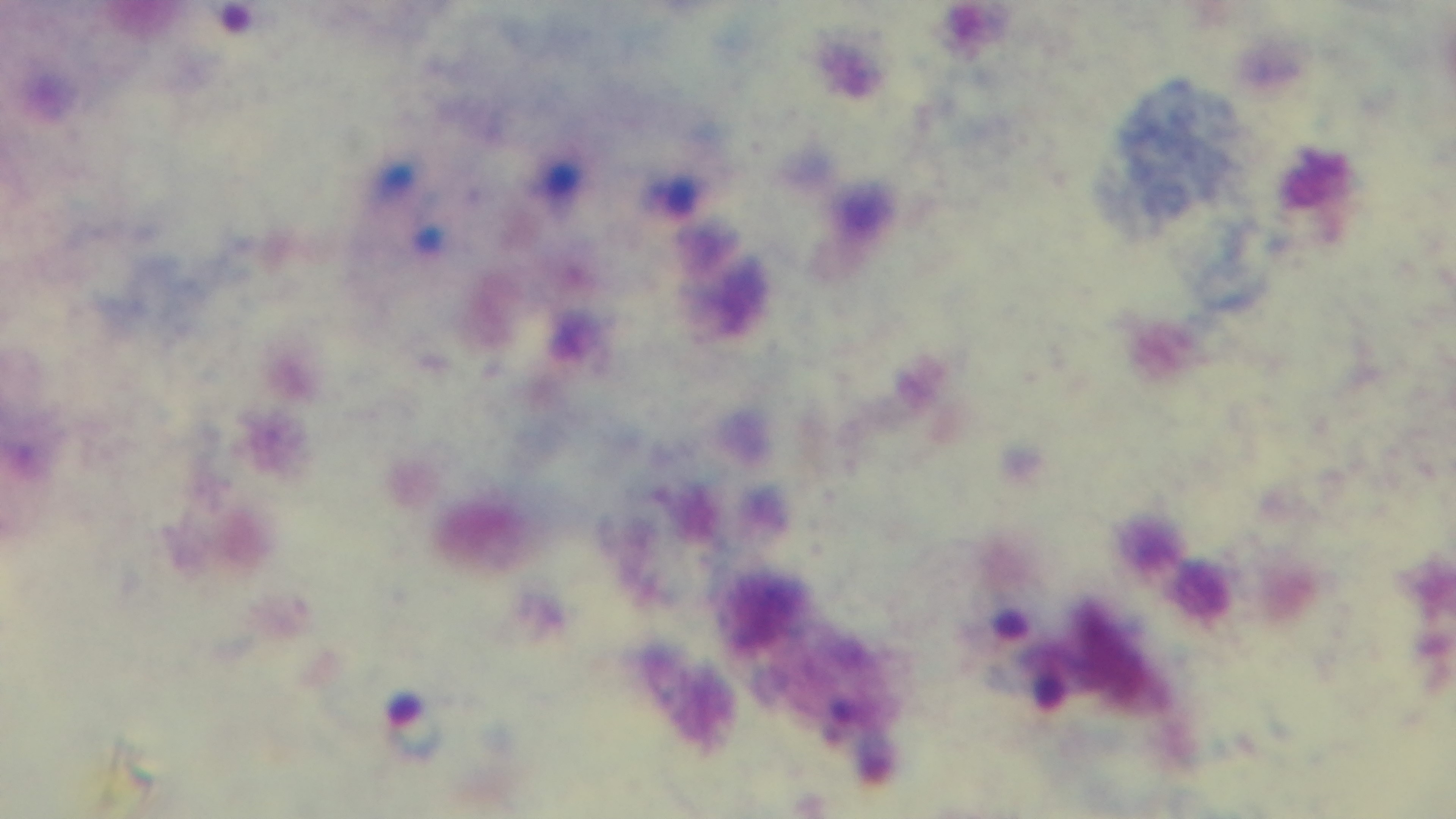

Summary:
  - Modality: light microscopy
  - Malaria status: positive
  - Capture: mounted 4K digital camera
  - Field of view: single
  - Objective: 100x oil immersion
  - Preparation: thick smear
  - Stain: Giemsa